Describe the morphology of the red blood cells.
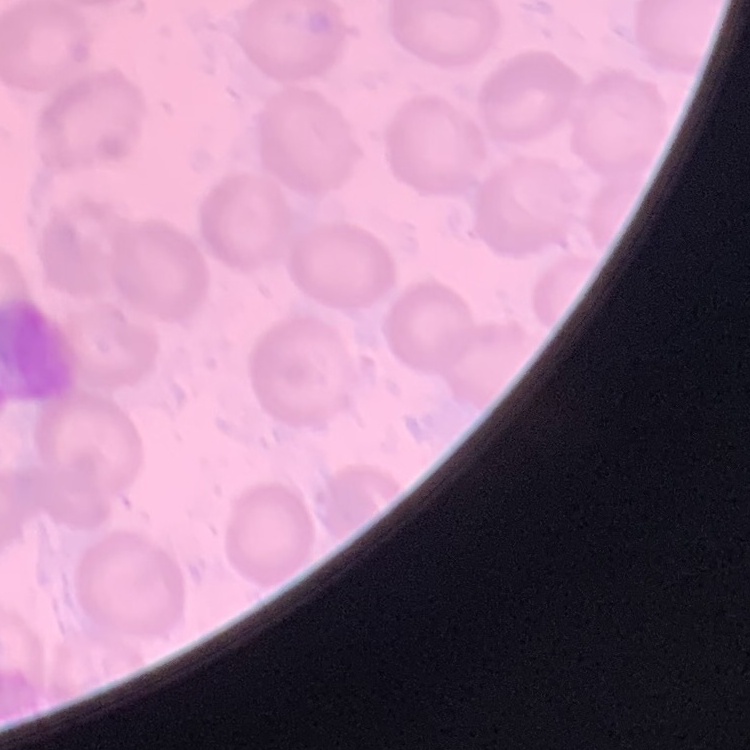
They show no rouleaux formation.

Thin blood smear. Square crop of a larger photomicrograph. Stained with either Field's or Giemsa.